Locate every Plasmodium parasite.
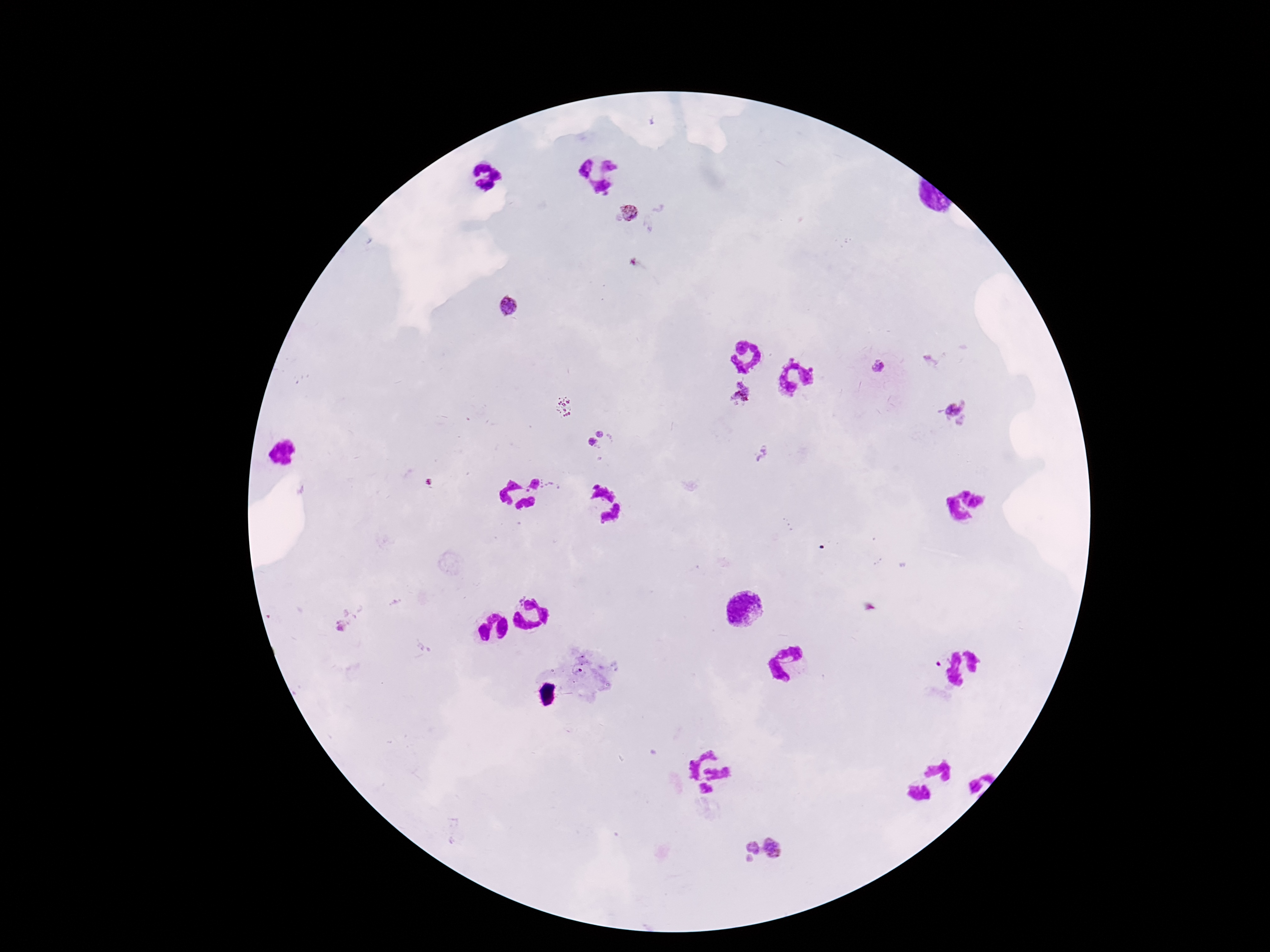
Approximate centers as (x, y) in pixels.
Plasmodium parasites: (631, 212), (510, 307), (879, 367), (742, 393), (958, 411), (606, 432), (592, 445), (779, 847), (747, 852).

Summary:
  - Preparation: thick blood film
  - Magnification: 100x
  - Stain: Giemsa
  - Patient malaria status: positive
  - Field of view: single
  - Capture: smartphone camera through the microscope eyepiece
  - Image size: 1270×952 pixels